Evaluate for malaria.
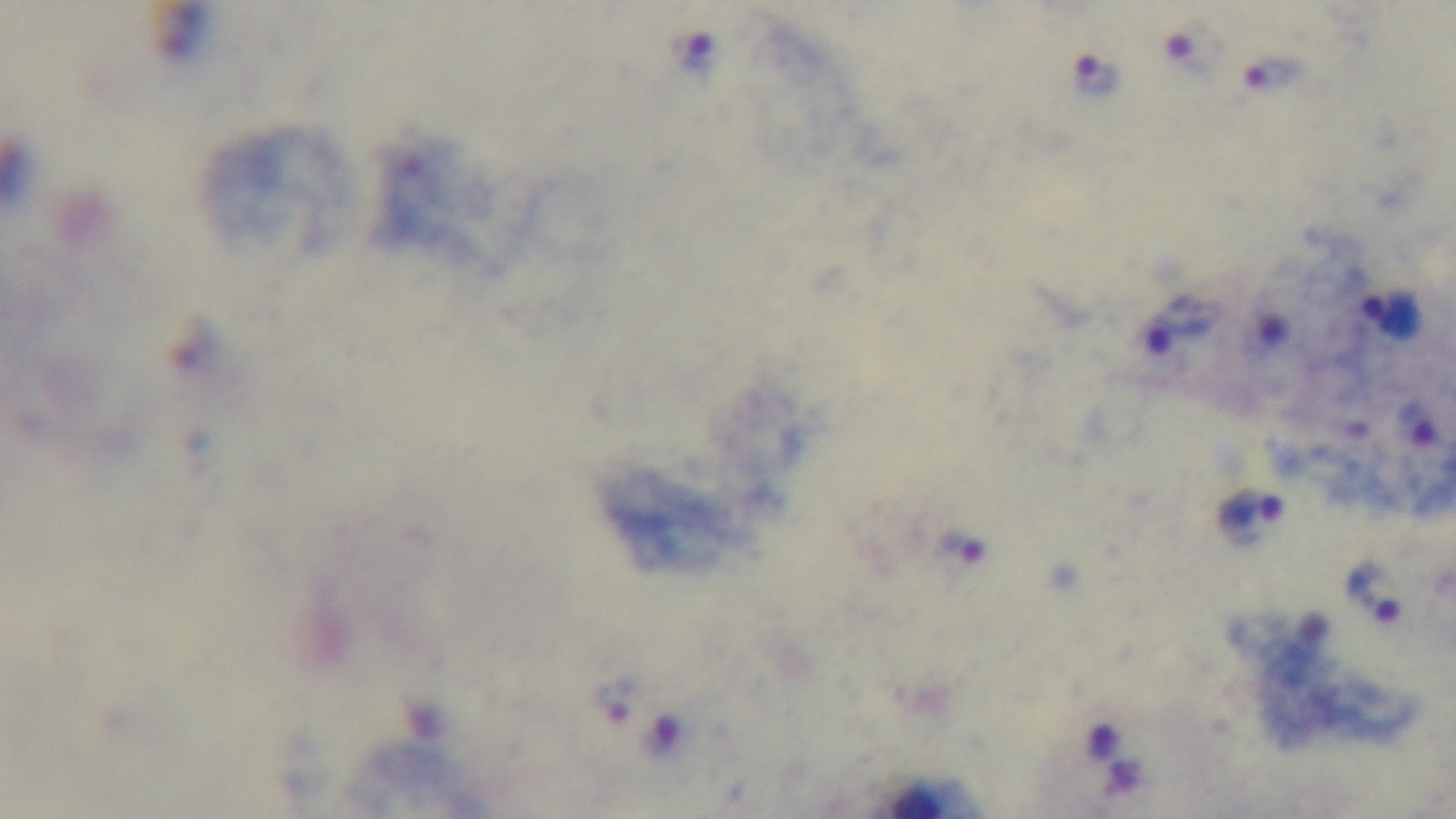
Infected.

Summary:
  - Field of view: one from the slide
  - Modality: light microscopy
  - Objective: 100x oil immersion
  - Capture: mounted 4K digital camera
  - Preparation: thick smear
  - Stain: Giemsa